Report the malaria status of this cell.
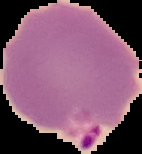

Parasitized.

Image is 142×154 pixels. From a thin blood film. Cell region segmented out of the field of view; the surrounding area is masked to black.